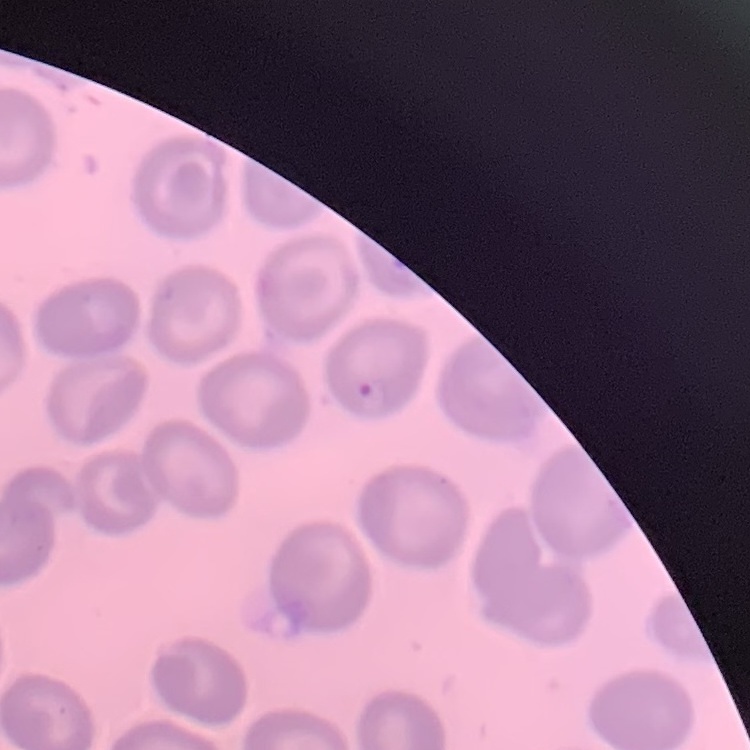

Summary:
  - Erythrocyte morphology: no rouleaux formation
  - Image type: square crop of a larger photomicrograph
  - Preparation: thin blood film
  - Stain: Field's or Giemsa